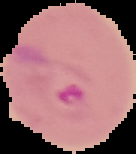 Image is 136×154 pixels. Result: malaria parasites detected. The area outside the segmented cell region is set to black. From a thin blood smear.